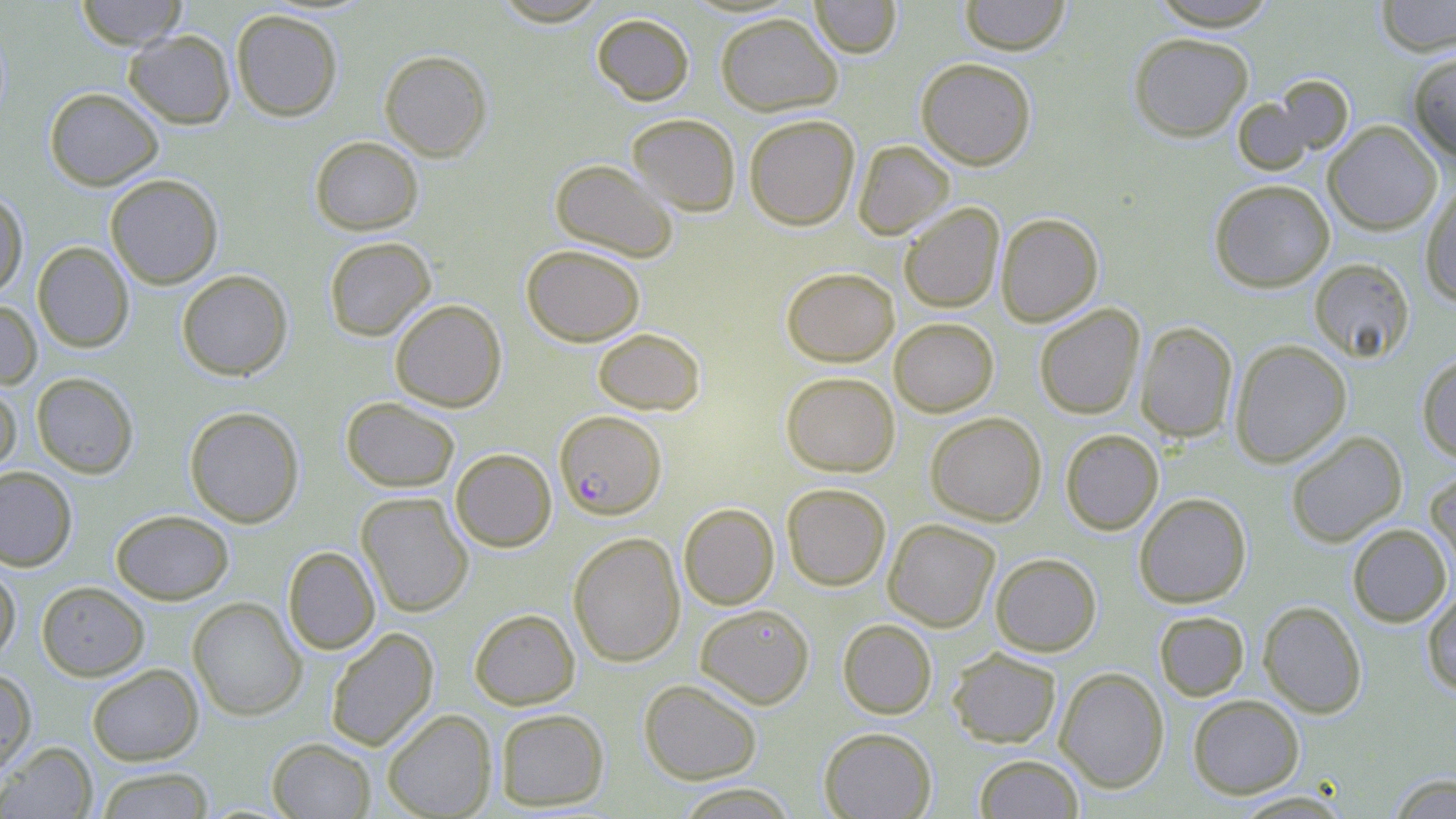

Summary:
  - Coordinate format: approximate bounding boxes as (x1, y1, x2, y2) in pixels
  - Plasmodium falciparum-infected red blood cell locations: (555, 414, 666, 523)
  - Uninfected red blood cell locations: (75, 0, 188, 49), (491, 0, 610, 26), (809, 0, 902, 58), (958, 0, 1071, 55), (1148, 0, 1281, 30), (1374, 0, 1456, 56), (231, 9, 343, 121), (591, 12, 694, 105), (715, 12, 842, 116), (124, 29, 236, 129), (1128, 32, 1254, 141), (379, 49, 493, 161), (1407, 51, 1456, 160), (916, 58, 1036, 170), (1232, 83, 1348, 174), (44, 87, 163, 190), (627, 113, 740, 216), (744, 114, 860, 230), (1323, 121, 1442, 235), (310, 136, 423, 235), (853, 140, 954, 239), (550, 159, 679, 262), (105, 173, 223, 289), (1209, 179, 1335, 292), (1421, 184, 1456, 307), (0, 190, 28, 299), (899, 202, 1004, 313), (996, 212, 1104, 326), (323, 237, 436, 341), (32, 242, 134, 352), (521, 244, 645, 346), (1309, 258, 1415, 363), (781, 266, 899, 366), (176, 270, 292, 380), (390, 298, 507, 412), (0, 299, 42, 390), (1034, 304, 1145, 420), (889, 317, 998, 416), (1135, 321, 1238, 442), (593, 327, 705, 415), (1229, 339, 1351, 467), (1416, 353, 1456, 463), (781, 371, 900, 477), (31, 372, 139, 478), (0, 381, 21, 478), (341, 397, 460, 492), (184, 406, 305, 528), (925, 412, 1047, 526), (1060, 429, 1164, 534), (1285, 430, 1407, 547), (450, 448, 557, 552), (0, 466, 77, 570), (1425, 466, 1456, 579), (781, 483, 891, 591), (356, 492, 474, 617), (1134, 492, 1251, 608), (678, 503, 779, 609), (110, 509, 234, 604), (883, 519, 1000, 632), (1347, 523, 1452, 627), (568, 532, 686, 666), (283, 546, 380, 654), (990, 552, 1102, 656), (0, 560, 20, 665), (36, 581, 150, 681), (1422, 586, 1456, 697), (187, 597, 306, 720), (1258, 600, 1368, 718), (695, 604, 814, 709), (469, 608, 580, 709), (1153, 610, 1249, 701), (837, 619, 937, 719), (325, 627, 439, 751), (947, 647, 1061, 748), (86, 663, 203, 765), (0, 667, 37, 778), (1054, 667, 1169, 793), (638, 678, 762, 783), (1187, 694, 1305, 798), (382, 708, 497, 819), (494, 708, 609, 811), (819, 727, 937, 819), (267, 737, 375, 818), (1, 741, 97, 819), (974, 753, 1084, 818), (95, 767, 215, 818), (1387, 773, 1456, 818), (673, 783, 801, 819), (1231, 791, 1355, 818)
  - Slide-level diagnosis: Plasmodium falciparum
  - Stain: May-Grünwald-Giemsa
  - Field of view: one of a larger specimen
  - Modality: optical microscopy
  - Image size: 1456×819 pixels
  - Preparation: thin blood film
  - Magnification: 1000x